Assess this cell for malaria.
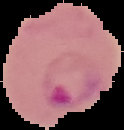
Parasitized.

Summary:
  - Preparation: thin blood film
  - Image size: 124×130 pixels
  - Image type: segmented cell region with the area outside set to black